Report the malaria status of this cell.
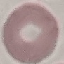
Uninfected.

Summary:
  - Preparation: thin blood smear
  - Capture: smartphone through the microscope eyepiece
  - Image type: cell patch, automatically extracted from a larger field of view and resized to 64 × 64 pixels
  - Stain: Giemsa